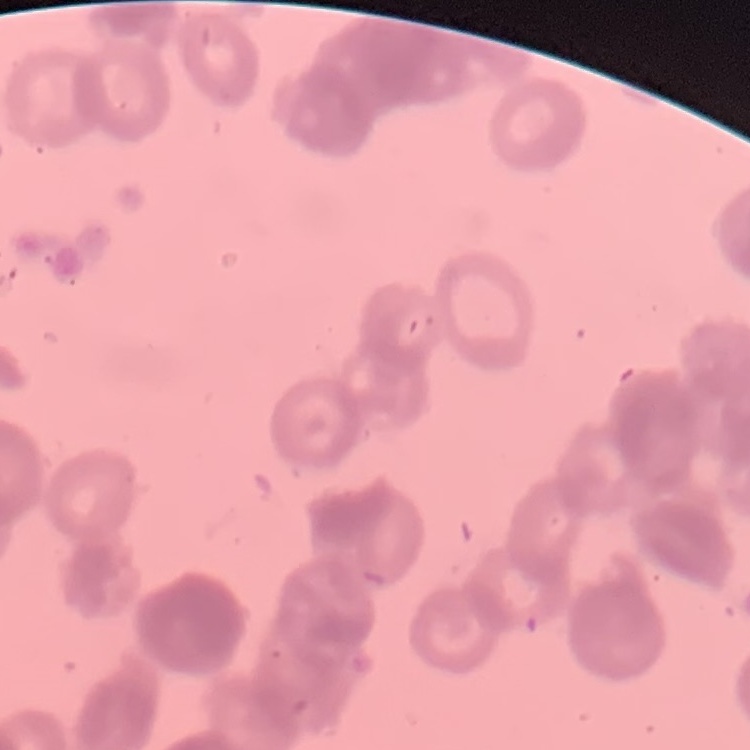

The red blood cells show rouleaux formation. Thin peripheral smear. Square crop of a larger photomicrograph. Field's or Giemsa stain.